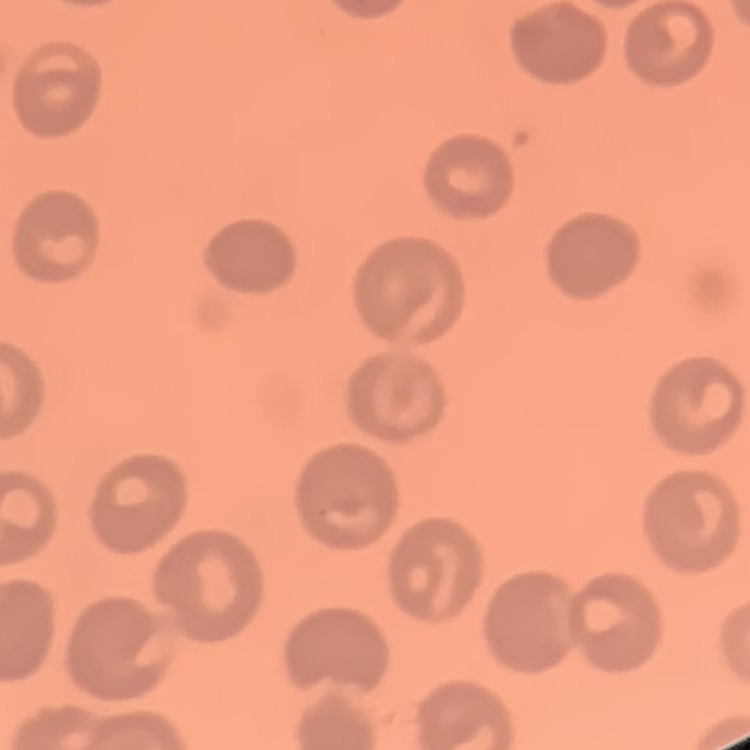

Summary:
  - Erythrocyte morphology: no rouleaux formation
  - Preparation: thin peripheral smear
  - Image type: one tile cut from a larger photomicrograph
  - Stain: Field's or Giemsa